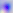

magnification: 400x
modality: photomicrograph
identification: Toxoplasma gondii